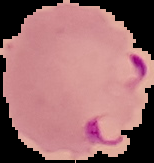
Malaria status: parasitized. From a thin blood film. Image is 154×163 pixels. Segmented cell region on a black background.